Outline every Plasmodium parasite, every leukocyte, and every artifact (stain precipitate or debris).
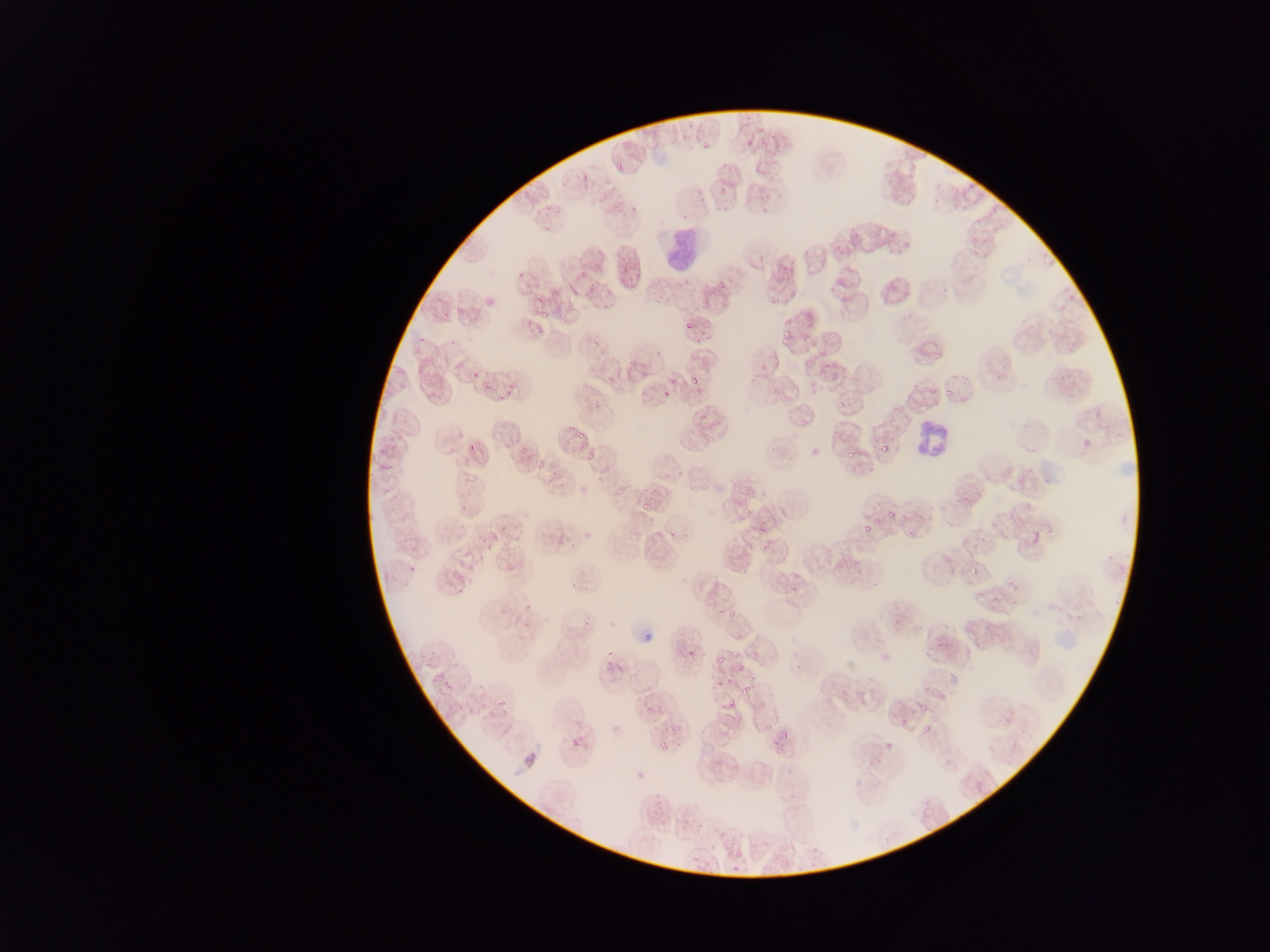

Approximate bounding boxes as left top right bottom in pixels.
Plasmodium parasites: 760 137 767 147; 702 139 717 149; 719 188 732 194; 547 197 556 212; 631 201 637 212; 902 240 911 250; 891 246 901 255; 617 252 630 270; 621 277 630 292; 526 279 534 289; 715 279 727 293; 771 288 783 306; 535 296 545 305; 589 296 596 304; 781 309 800 338; 540 310 550 315; 537 325 547 336; 685 325 696 334; 934 347 941 358; 803 350 817 367; 773 358 787 369; 759 361 769 371; 469 366 483 382; 689 374 700 384; 670 377 679 384; 941 381 952 398; 661 389 668 398; 693 389 702 394; 493 390 504 403; 504 391 513 397; 960 393 969 402; 891 398 901 414; 835 399 845 409; 562 423 577 432; 451 428 461 438; 576 429 586 443; 703 430 713 446; 560 435 572 444; 467 438 481 449; 889 438 899 456; 881 443 889 462; 845 445 855 460; 850 468 859 475; 963 491 974 502; 642 496 651 511; 887 501 896 516; 761 504 772 513; 647 514 657 523; 757 522 767 535; 863 523 874 533; 905 526 917 541; 1001 526 1010 539; 1027 528 1044 548; 509 529 518 543; 511 547 523 556; 758 548 766 555; 970 552 980 571; 494 556 507 567; 1007 574 1019 588; 971 588 988 606; 521 603 530 612; 1076 604 1089 622; 719 607 724 620; 730 609 742 622; 642 630 655 644; 686 640 697 657; 605 647 612 659; 924 647 930 660; 715 654 724 664; 605 658 615 668; 736 668 745 674; 712 682 725 691; 441 683 449 692; 742 687 757 695; 497 698 510 713; 722 702 740 712; 919 702 927 712; 764 723 772 733; 923 724 933 733; 571 736 583 750; 658 741 673 752; 969 778 986 797; 780 854 793 872; 732 862 744 874 | approximate x y pixel centers of objects too small to bound: 617 171; 562 321; 776 352; 587 455; 747 491; 1110 558; 458 595; 729 680; 784 739; 886 745; 738 854.
Leukocytes: 661 224 705 277; 908 410 944 463.

Summary:
  - Country: Ghana
  - Field of view: single
  - Preparation: thin blood smear
  - Image size: 1270×952 pixels
  - Capture: mobile-phone photograph through a microscope